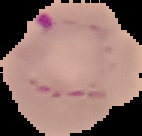

Summary:
  - Result: malaria parasites identified
  - Image size: 142×136 pixels
  - Preparation: thin blood smear
  - Image type: segmented cell region with the area outside set to black